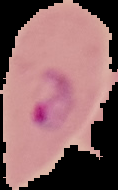

Summary:
  - Preparation: thin blood film
  - Image type: segmented cell region with the area outside set to black
  - Image size: 118×190 pixels
  - Malaria status: parasitized